Report the malaria status of this cell.
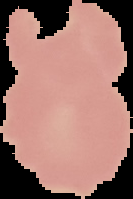

It is uninfected.

Image is 133×199 pixels. From a thin blood smear. The area outside the segmented cell region is set to black.